Give the extent of all Babesia divergens-infected red blood cells.
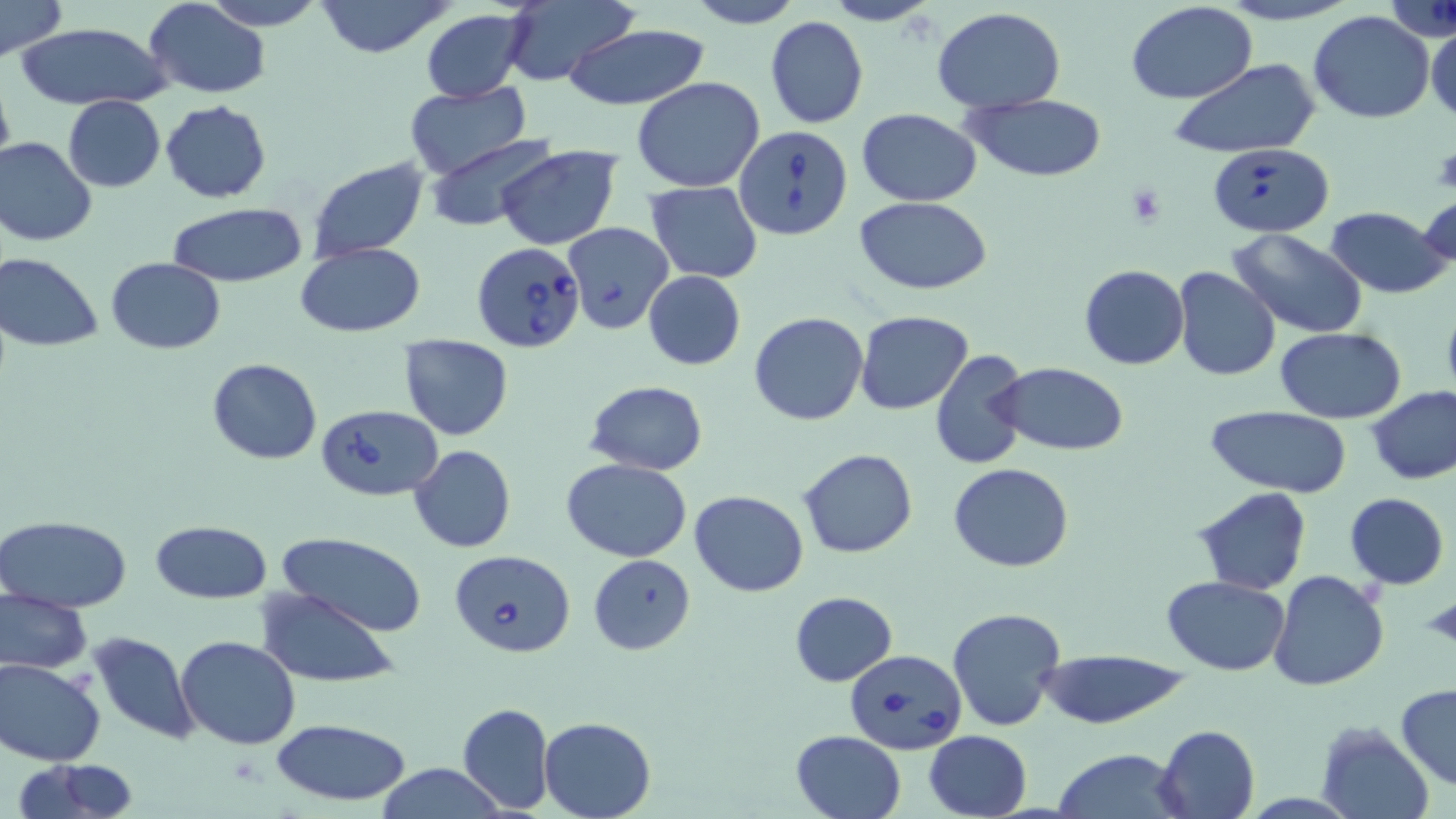
Approximate bounding boxes as [x1, y1, x2, y2] in pixels.
Babesia divergens-infected red blood cells: [733, 122, 853, 239], [1209, 142, 1333, 235], [471, 240, 587, 353], [316, 405, 442, 503], [448, 548, 576, 656], [844, 649, 965, 756].

Uninfected red blood cell locations: [1, 0, 68, 61], [143, 0, 271, 100], [199, 0, 329, 30], [313, 0, 458, 58], [680, 0, 805, 28], [821, 0, 941, 27], [1215, 0, 1361, 26], [499, 2, 636, 88], [1125, 2, 1258, 105], [933, 7, 1065, 112], [422, 10, 530, 104], [1308, 11, 1435, 125], [765, 15, 869, 129], [16, 21, 173, 111], [564, 23, 707, 110], [1426, 23, 1456, 124], [1172, 58, 1320, 161], [0, 74, 15, 175], [631, 76, 766, 191], [404, 84, 531, 180], [965, 93, 1107, 182], [63, 96, 166, 192], [160, 100, 271, 202], [858, 108, 982, 206], [428, 135, 557, 233], [0, 136, 98, 246], [496, 146, 621, 250], [307, 156, 431, 262], [644, 181, 763, 283], [1417, 194, 1456, 279], [854, 196, 993, 293], [167, 202, 307, 289], [1324, 207, 1449, 299], [562, 222, 675, 334], [1228, 228, 1368, 341], [294, 243, 424, 337], [1, 252, 103, 350], [106, 257, 227, 353], [1079, 265, 1188, 369], [1172, 266, 1281, 382], [643, 270, 746, 370], [855, 310, 973, 415], [750, 312, 869, 425], [1275, 329, 1406, 423], [397, 333, 516, 440], [930, 347, 1030, 470], [207, 358, 323, 464], [992, 362, 1128, 455], [584, 380, 708, 475], [1367, 385, 1456, 485], [1204, 405, 1353, 495], [409, 445, 515, 553], [797, 448, 918, 560], [560, 458, 693, 562], [949, 463, 1074, 571], [1193, 487, 1310, 596], [690, 490, 810, 597], [1344, 493, 1449, 589], [1, 513, 134, 612], [151, 519, 273, 603], [277, 533, 427, 637], [589, 553, 694, 655], [1270, 569, 1389, 691], [1161, 575, 1289, 674], [255, 587, 404, 688], [0, 588, 95, 674], [788, 591, 897, 687], [947, 607, 1067, 731], [90, 631, 199, 745], [176, 636, 302, 749], [1041, 649, 1187, 728], [1, 657, 106, 766], [1395, 684, 1456, 792], [456, 702, 555, 815], [539, 717, 655, 819], [271, 718, 411, 808], [1316, 721, 1434, 819], [1155, 724, 1260, 819], [790, 730, 907, 819], [924, 731, 1032, 819], [1055, 747, 1188, 819], [12, 760, 141, 819], [373, 763, 511, 819]. Platelet locations: [1123, 184, 1170, 227], [1421, 592, 1456, 654]. Slide-level diagnosis: Babesia divergens. 1000x magnification. Light microscopy. Image is 1456×819 pixels. May-Grünwald-Giemsa-stained preparation. Thin blood film. One field of a larger specimen.